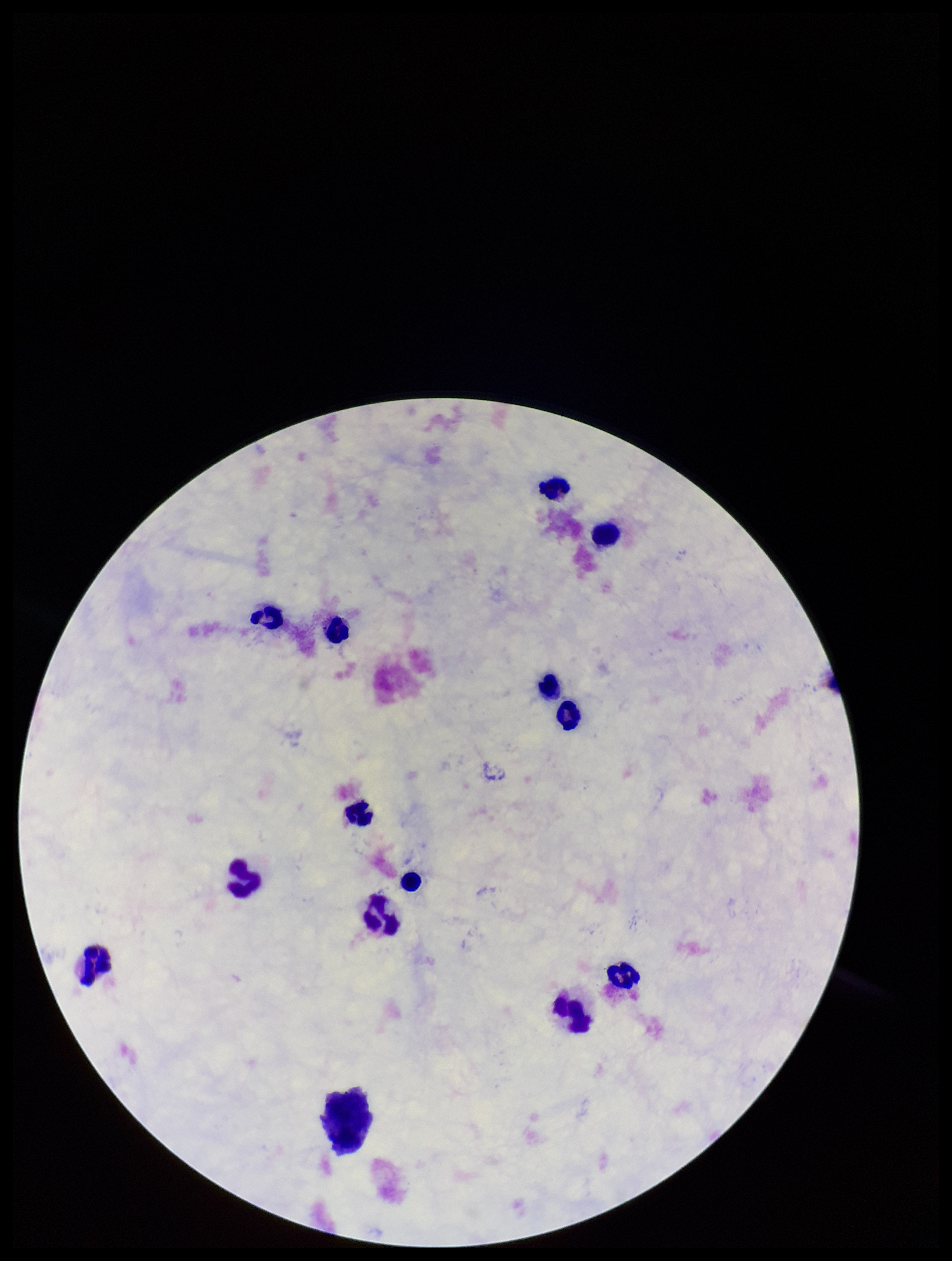
field of view = single
Plasmodium parasites = none detected
leukocyte count = 18
stain = Giemsa
capture = smartphone photograph through the microscope eyepiece
image size = 952×1261 pixels
parasite count = 0
patient malaria status = negative
preparation = thick blood smear